Give the extent of all white blood cells.
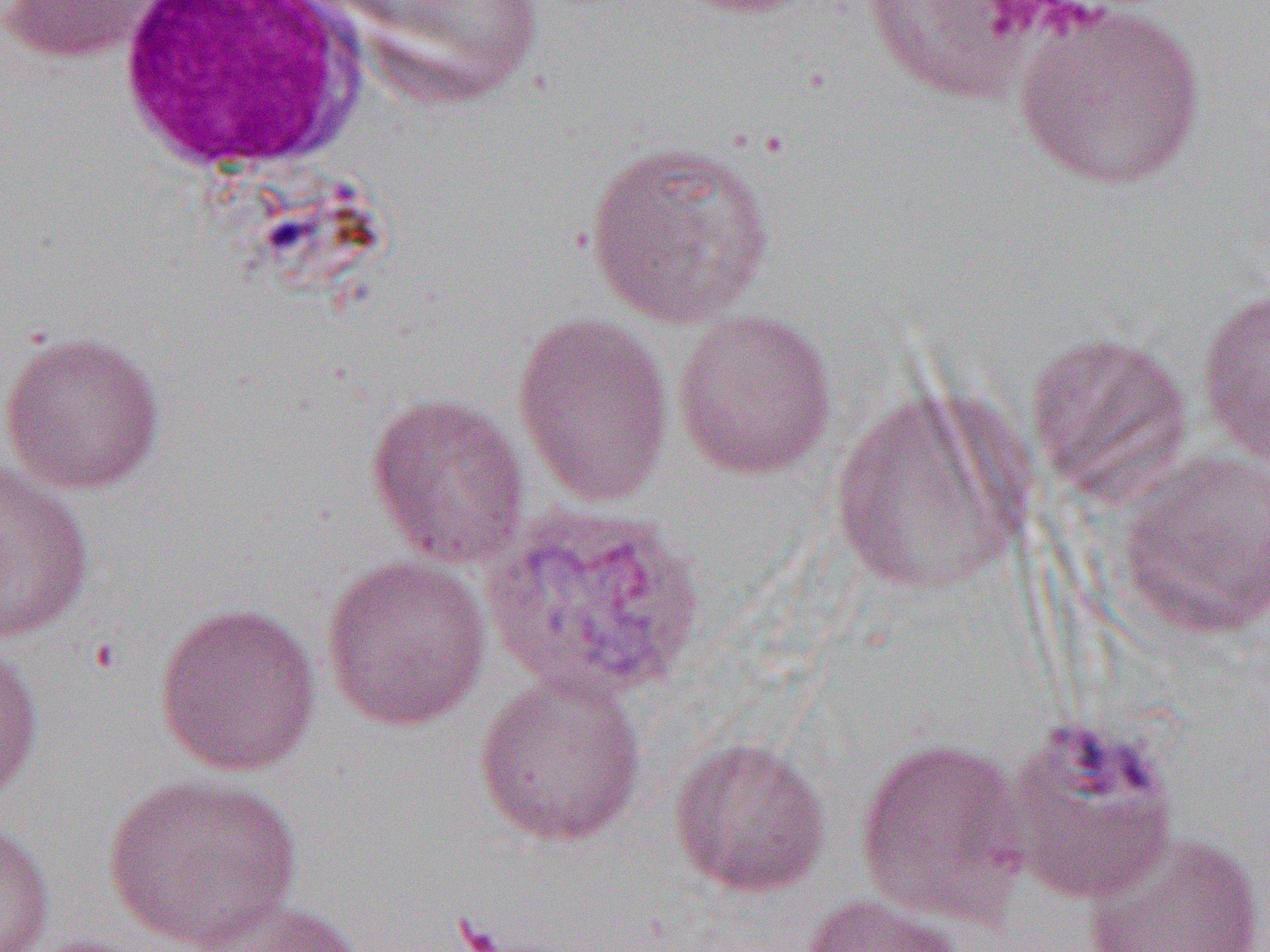

Approximate bounding boxes as named x1/y1/x2/y2 corners in pixels.
White blood cells: (x1=115, y1=1, x2=374, y2=174).

Uninfected red blood cell locations: (x1=0, y1=0, x2=168, y2=63), (x1=339, y1=0, x2=546, y2=112), (x1=662, y1=0, x2=820, y2=18), (x1=860, y1=1, x2=1046, y2=105), (x1=1011, y1=2, x2=1206, y2=190), (x1=582, y1=138, x2=776, y2=329), (x1=1196, y1=287, x2=1270, y2=470), (x1=671, y1=307, x2=838, y2=480), (x1=512, y1=311, x2=675, y2=506), (x1=0, y1=329, x2=166, y2=495), (x1=1025, y1=329, x2=1193, y2=501), (x1=829, y1=388, x2=1027, y2=595), (x1=365, y1=391, x2=532, y2=571), (x1=1117, y1=450, x2=1270, y2=638), (x1=0, y1=461, x2=94, y2=644), (x1=320, y1=554, x2=492, y2=731), (x1=153, y1=602, x2=323, y2=777), (x1=0, y1=637, x2=44, y2=801), (x1=472, y1=672, x2=648, y2=848), (x1=1001, y1=716, x2=1181, y2=903), (x1=669, y1=736, x2=832, y2=898), (x1=853, y1=736, x2=1031, y2=925), (x1=102, y1=772, x2=303, y2=951), (x1=0, y1=822, x2=55, y2=952), (x1=1082, y1=829, x2=1267, y2=951), (x1=798, y1=892, x2=966, y2=952), (x1=189, y1=898, x2=365, y2=952). Slide-level diagnosis: Plasmodium vivax. Image is 1270×952 pixels. One field of a larger specimen. 1000x magnification. Thin blood smear. Optical microscopy.